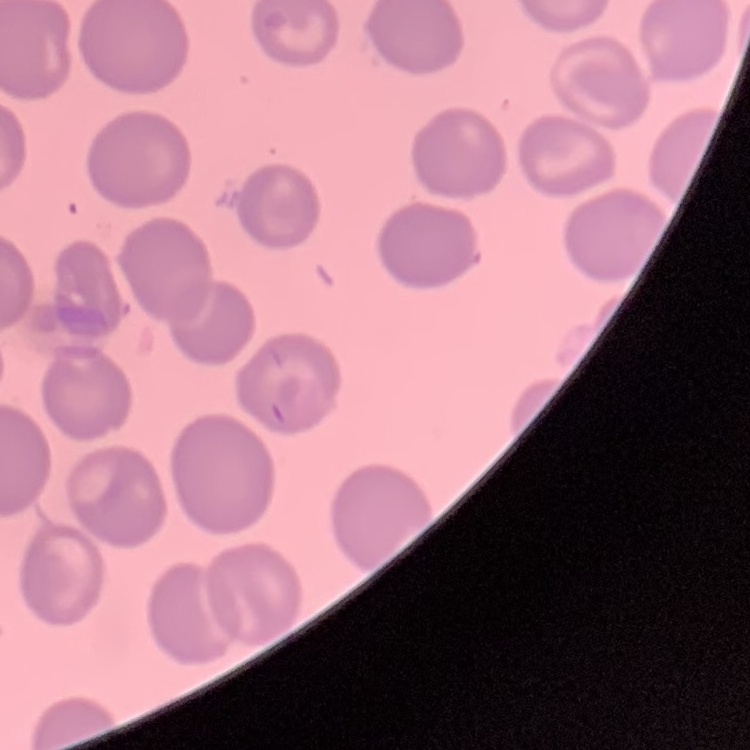
{
  "red_blood_cell_morphology": "no rouleaux formation",
  "stain": "Field's or Giemsa",
  "image_type": "square crop of a larger photomicrograph",
  "preparation": "thin blood smear"
}